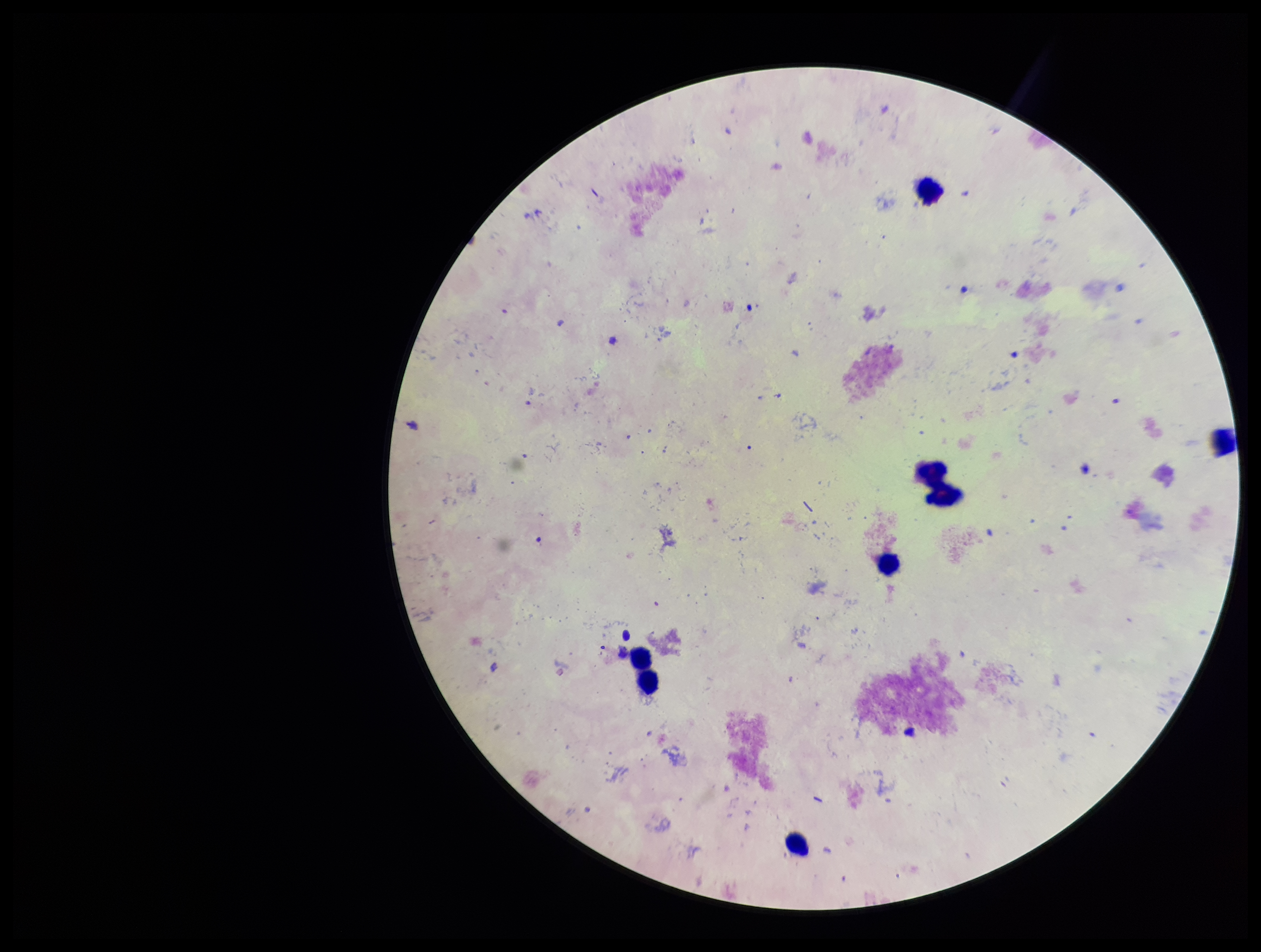

Preparation: thick smear. Leukocyte count: 6. Plasmodium parasites: none detected. Parasite count: 0. Stained with Giemsa. Single field of view. Patient malaria status: negative. Image is 1261×952 pixels. Photographed through the microscope eyepiece with a smartphone camera.